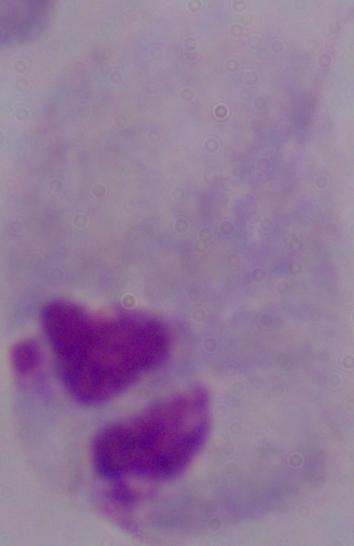

magnification = 1000x
identification = trichomonad
modality = photomicrograph